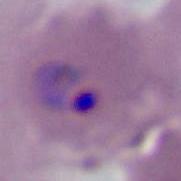

magnification = 400x or 1000x
modality = photomicrograph
identification = Plasmodium